Comment on the morphology of the red blood cells.
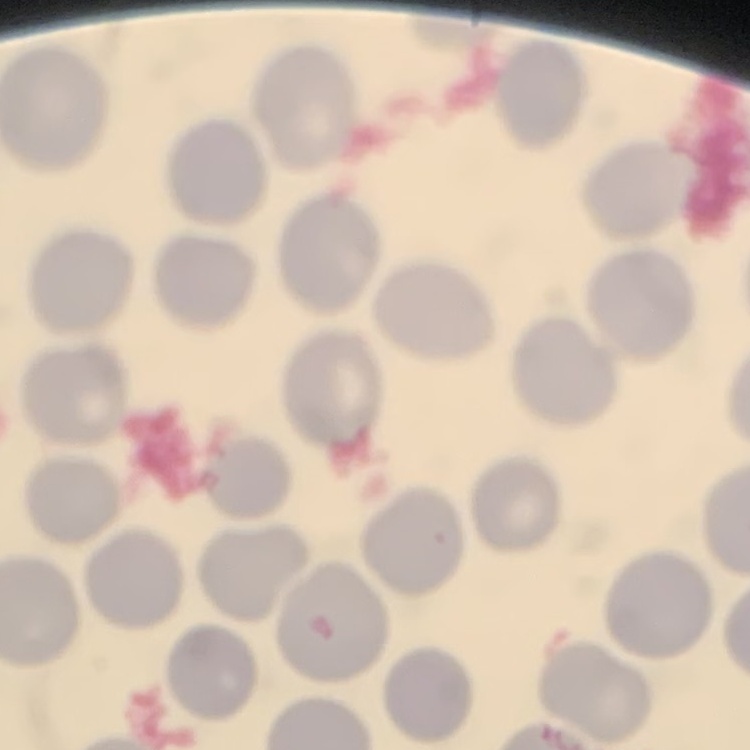

They show no rouleaux formation.

stain = Field's or Giemsa
preparation = thin blood smear
image type = one tile cut from a larger photomicrograph